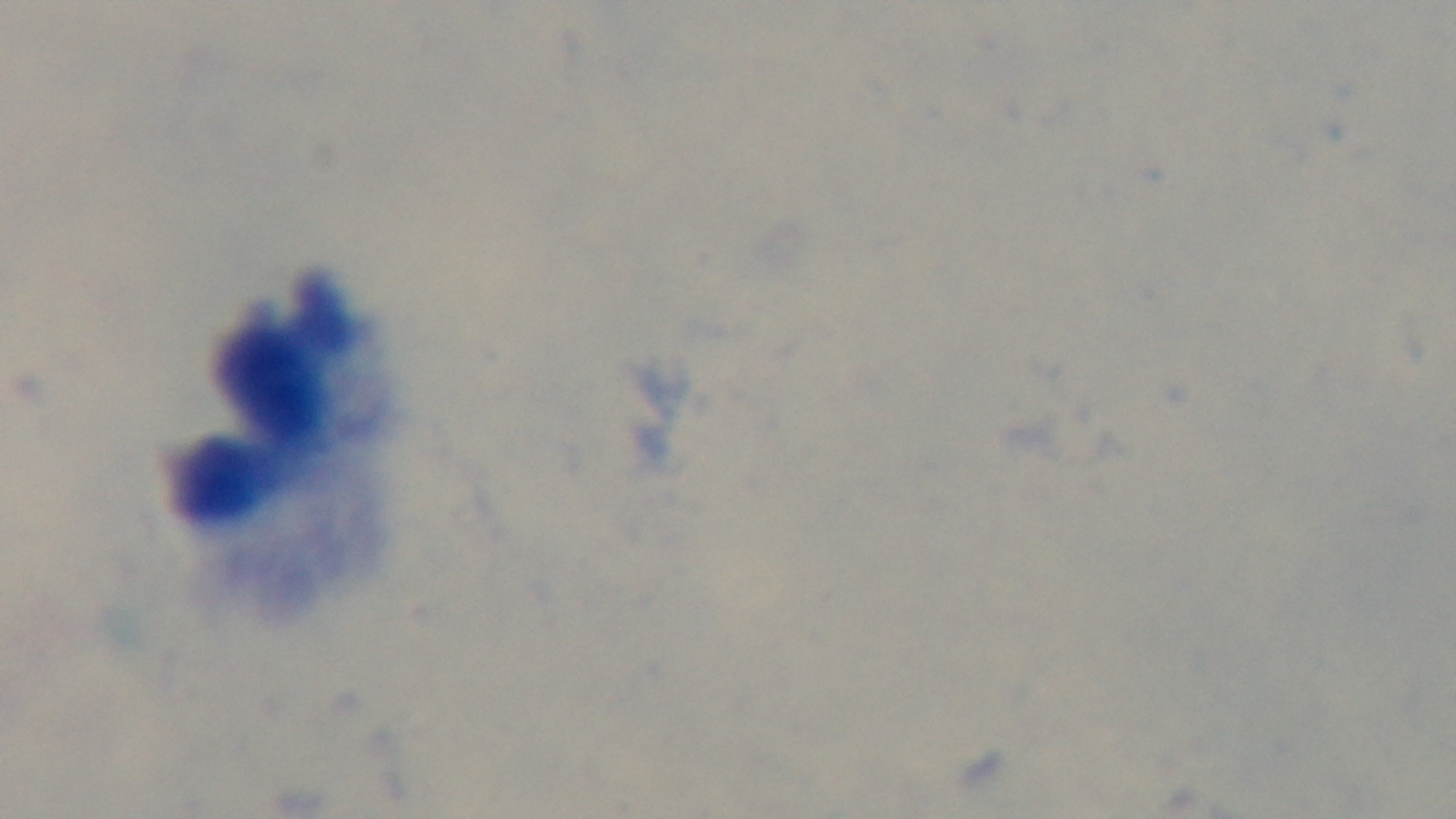

Summary:
  - Capture: mounted 4K digital camera
  - Objective: 100x oil immersion
  - Modality: light microscopy
  - Preparation: thick
  - Stain: Giemsa
  - Field of view: single
  - Malaria status: negative